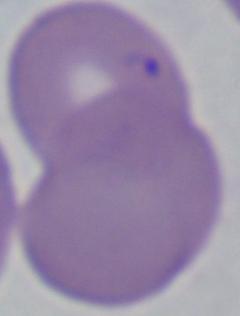

Summary:
  - Magnification: 1000x
  - Identification: Babesia
  - Modality: photomicrograph